Name the cell type shown.
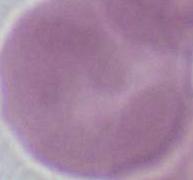
This is an erythrocyte.

Summary:
  - Magnification: 1000x
  - Modality: photomicrograph